State the blood parasite species.
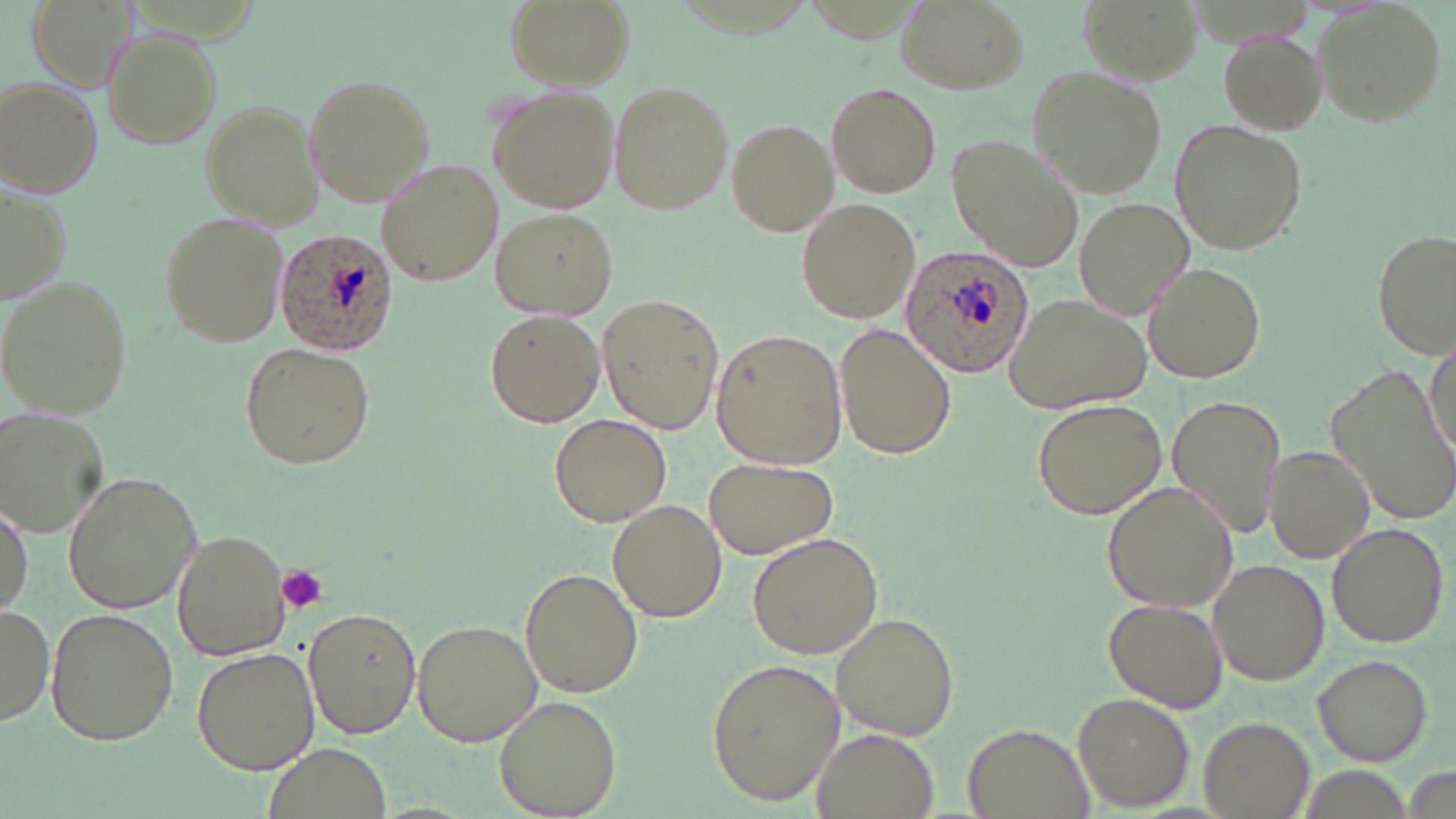
Plasmodium ovale.

Approximate bounding boxes as [x1, y1, x2, y2] in pixels. Platelet locations: [277, 567, 328, 612]. Uninfected red blood cell locations: [505, 0, 631, 90], [895, 1, 1027, 95], [1311, 3, 1449, 126], [1216, 28, 1327, 133], [102, 29, 221, 150], [1027, 65, 1170, 198], [303, 73, 436, 208], [1, 77, 105, 197], [607, 82, 734, 216], [826, 82, 941, 198], [488, 86, 622, 214], [199, 99, 323, 227], [726, 119, 836, 235], [1171, 121, 1306, 256], [946, 135, 1084, 274], [377, 159, 502, 287], [1, 183, 72, 306], [795, 196, 920, 324], [1074, 197, 1195, 320], [492, 208, 617, 319], [157, 210, 291, 347], [1373, 228, 1454, 358], [1144, 261, 1266, 385], [0, 275, 134, 420], [596, 295, 725, 434], [1005, 296, 1147, 412], [484, 310, 604, 427], [835, 322, 957, 460], [709, 328, 847, 472], [1425, 334, 1455, 460], [239, 341, 376, 471], [1327, 364, 1456, 523], [1167, 395, 1284, 539], [1030, 397, 1167, 519], [1, 410, 107, 536], [549, 412, 672, 528], [1265, 446, 1373, 559], [703, 456, 839, 560], [62, 471, 202, 615], [1102, 481, 1239, 613], [608, 499, 725, 623], [0, 502, 32, 622], [1325, 523, 1449, 649], [172, 529, 291, 660], [746, 531, 883, 660], [1206, 560, 1329, 689], [520, 567, 643, 697], [1104, 596, 1226, 713], [0, 602, 55, 729], [303, 605, 422, 740], [44, 607, 179, 745], [830, 611, 960, 741], [411, 618, 543, 747], [192, 647, 319, 774], [1313, 654, 1434, 765], [706, 658, 845, 806], [1071, 693, 1196, 812], [493, 694, 622, 818], [1197, 715, 1316, 818], [962, 724, 1096, 819], [809, 730, 939, 819], [259, 744, 395, 819]. Plasmodium ovale-infected red blood cell locations: [275, 229, 399, 356], [900, 243, 1033, 378]. Thin blood film. Optical microscopy. One field of a larger specimen. Image is 1456×819 pixels. May-Grünwald-Giemsa stain. Captured at 1000x magnification.